Assess this cell for malaria.
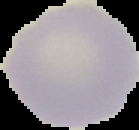

It is uninfected.

image_size: 139×130 pixels
image_type: segmented cell region with the area outside set to black
preparation: thin blood film